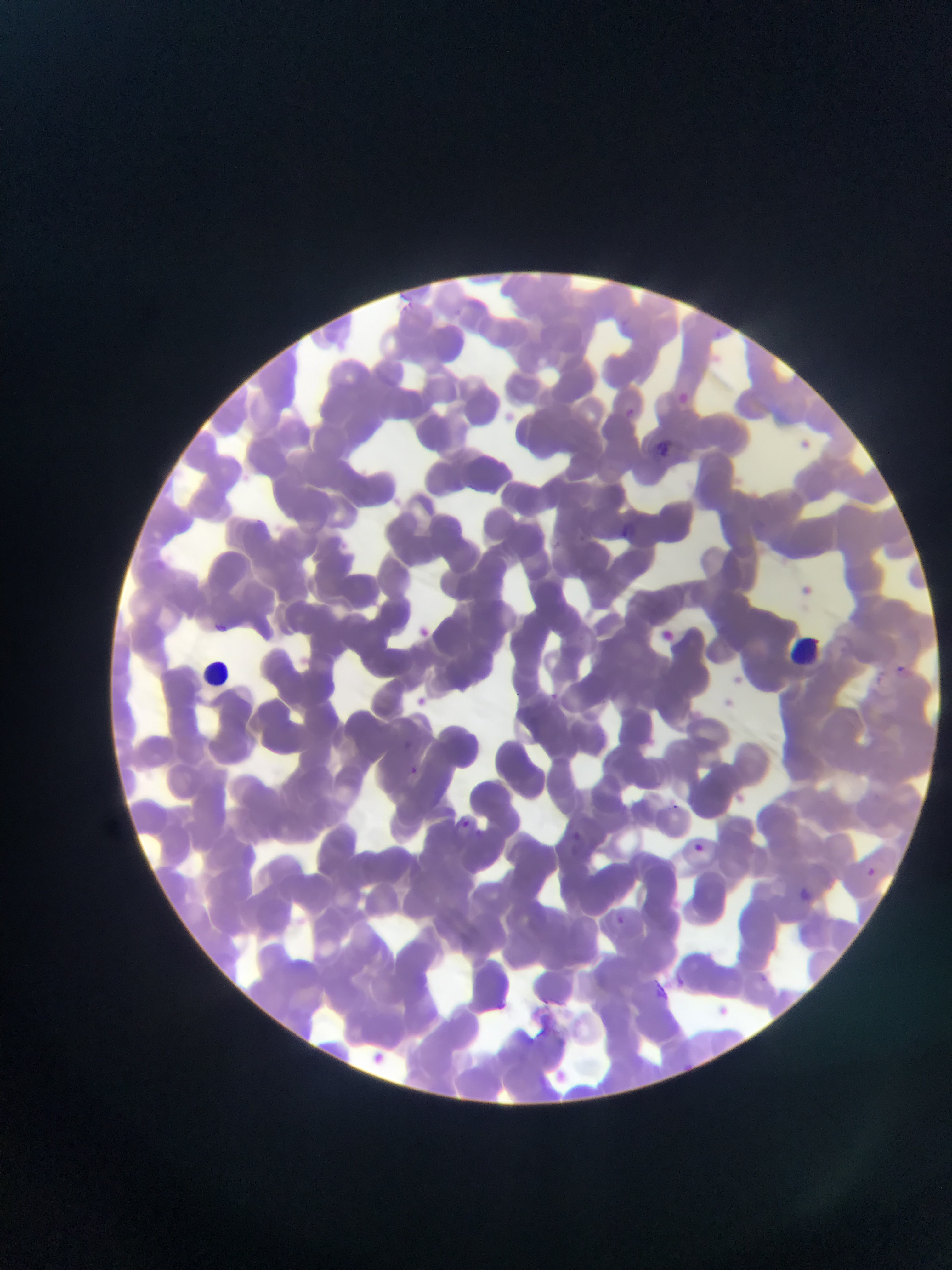
Approximate bounding boxes as left top right bottom in pixels. Malaria parasite locations: 682 390 691 404; 625 407 636 417; 659 439 677 458; 621 520 633 539; 215 623 231 635; 896 662 908 673; 550 689 558 701; 402 740 412 749; 411 766 418 775; 462 819 471 827; 573 829 584 842; 475 830 483 837; 694 841 705 852; 867 866 876 875; 800 885 813 901; 616 914 625 926; 759 971 769 983; 675 976 686 988; 649 977 670 1001 | approximate x y pixel centers of objects too small to bound: 719 333. Leukocyte locations: 792 634 826 666; 203 660 231 687. Mobile-phone photograph taken through the microscope. Image is 952×1270 pixels. Sample from Ghana. Thin blood film. Single field of view.